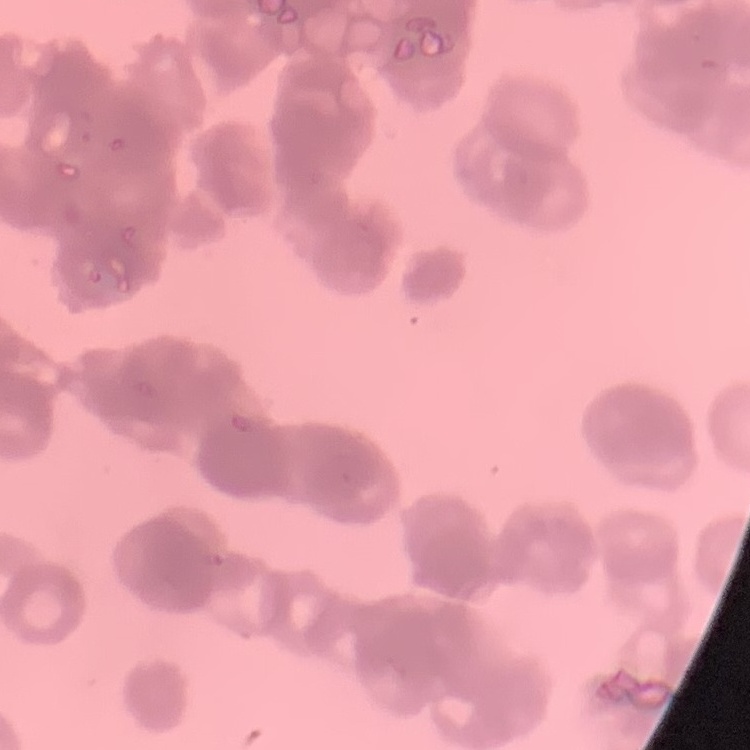

The red blood cells exhibit rouleaux formation. One tile cut from a larger photomicrograph. Field's or Giemsa stain. Thin peripheral smear.